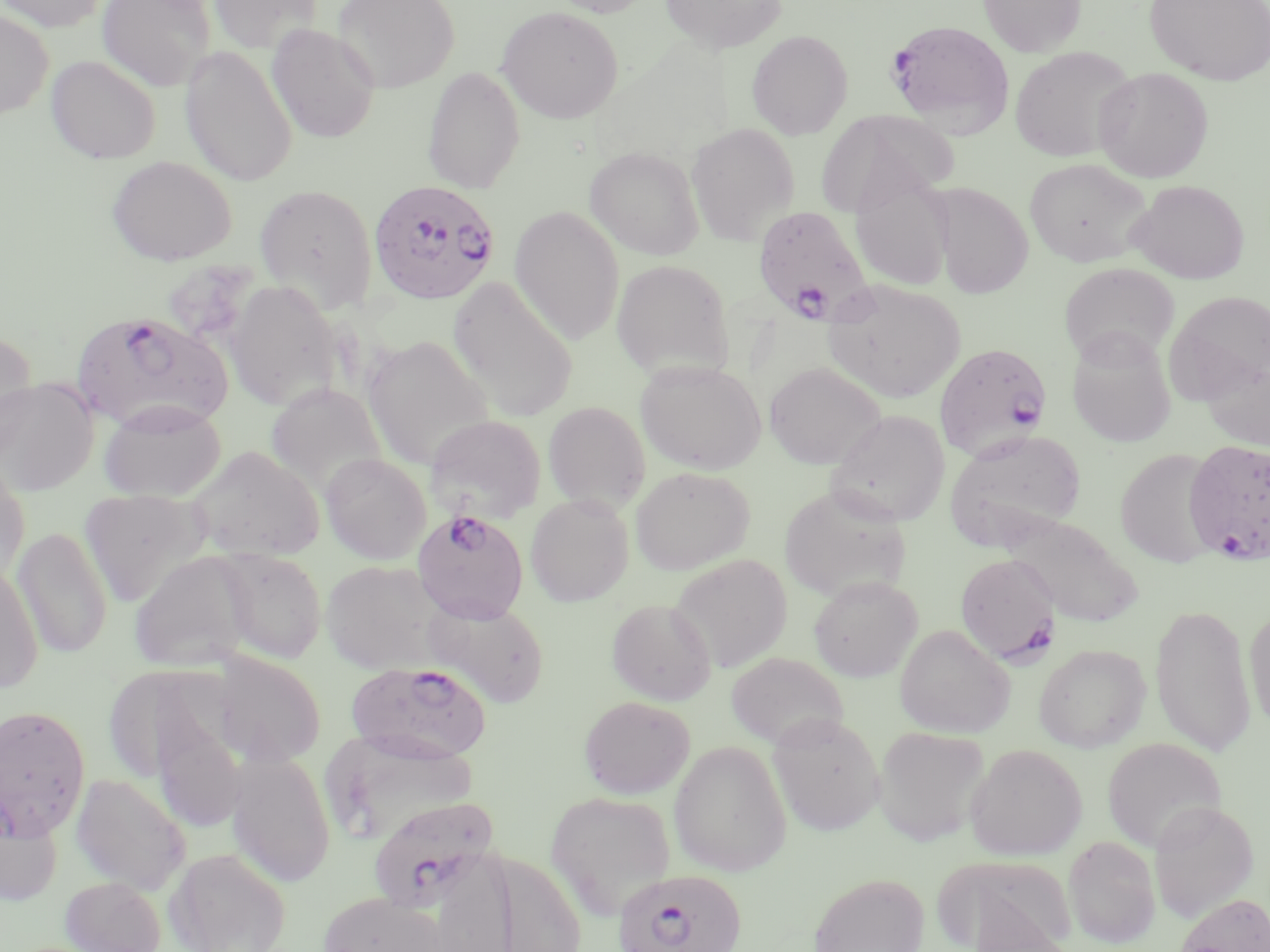
Summary:
  - Coordinate format: approximate bounding boxes as (x1,y1)-(x2,y2) corner pairs in pixels
  - Plasmodium falciparum-infected red blood cell locations: (887,19)-(1015,136), (368,179)-(501,304), (751,205)-(875,328), (72,310)-(232,432), (934,343)-(1053,461), (1184,439)-(1270,564), (413,508)-(528,623), (955,553)-(1059,666), (347,661)-(492,763), (366,796)-(499,912), (612,868)-(747,952)
  - Uninfected red blood cell locations: (0,0)-(107,32), (96,0)-(216,91), (208,0)-(323,55), (332,0)-(459,92), (544,0)-(656,17), (660,0)-(787,54), (978,0)-(1086,58), (1145,0)-(1270,84), (496,5)-(624,123), (0,11)-(53,117), (267,24)-(381,144), (746,30)-(853,139), (180,45)-(298,187), (1009,46)-(1137,162), (47,55)-(161,164), (422,66)-(525,193), (1094,67)-(1213,183), (815,109)-(955,218), (686,122)-(799,245), (585,147)-(704,260), (106,155)-(236,266), (1024,158)-(1151,267), (850,173)-(955,292), (1129,180)-(1249,283), (254,183)-(378,313), (932,184)-(1033,299), (509,205)-(626,344), (611,259)-(733,379), (1059,263)-(1179,367), (448,277)-(578,421), (223,279)-(342,410), (822,280)-(966,403), (1167,292)-(1270,398), (1067,329)-(1176,447), (0,330)-(37,452), (363,335)-(496,470), (1202,356)-(1270,450), (635,360)-(766,474), (764,362)-(885,469), (0,377)-(99,496), (265,384)-(386,497), (98,399)-(227,502), (543,401)-(650,512), (827,409)-(950,526), (426,414)-(546,523), (945,430)-(1085,550), (186,446)-(325,561), (1115,448)-(1220,567), (320,452)-(432,564), (0,459)-(30,585), (631,466)-(755,574), (777,483)-(913,603), (79,489)-(210,606), (526,493)-(634,606), (1003,513)-(1143,626), (13,526)-(113,657), (217,549)-(327,664), (129,551)-(254,672), (670,553)-(793,673), (321,560)-(448,674), (0,561)-(43,693), (809,575)-(922,681), (424,598)-(550,708), (607,599)-(716,704), (1150,603)-(1255,756), (1245,606)-(1270,731), (895,624)-(1014,737), (1033,643)-(1151,752), (726,651)-(847,750), (212,652)-(326,767), (579,695)-(695,799), (0,704)-(91,841), (153,708)-(246,834), (768,712)-(885,836), (873,726)-(990,846), (325,731)-(486,846), (1102,737)-(1227,853), (669,740)-(791,877), (965,743)-(1087,860), (227,750)-(335,887), (70,774)-(191,895), (545,790)-(677,916), (1149,799)-(1258,922), (0,807)-(62,908), (1064,835)-(1160,949), (166,847)-(291,952), (441,852)-(604,952), (942,857)-(1077,952), (808,872)-(929,952), (60,876)-(166,952), (316,891)-(452,952), (1173,893)-(1270,952)
  - Slide-level diagnosis: Plasmodium falciparum
  - Preparation: thin blood smear
  - Stain: May-Grünwald-Giemsa
  - Image size: 1270×952 pixels
  - Modality: light microscopy
  - Magnification: 1000x
  - Field of view: single